Report the malaria status of this cell.
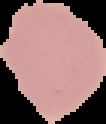
Uninfected.

Summary:
  - Image size: 106×124 pixels
  - Image type: cell region segmented out of the field of view; surrounding area masked to black
  - Preparation: thin blood smear